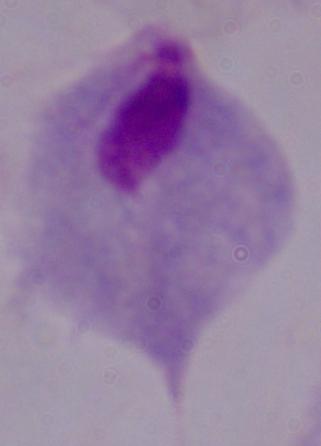

1000x magnification. A trichomonad is seen. Micrograph.